Identify the parasite.
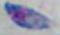

Toxoplasma gondii.

Photomicrograph. Captured at 1000x magnification.